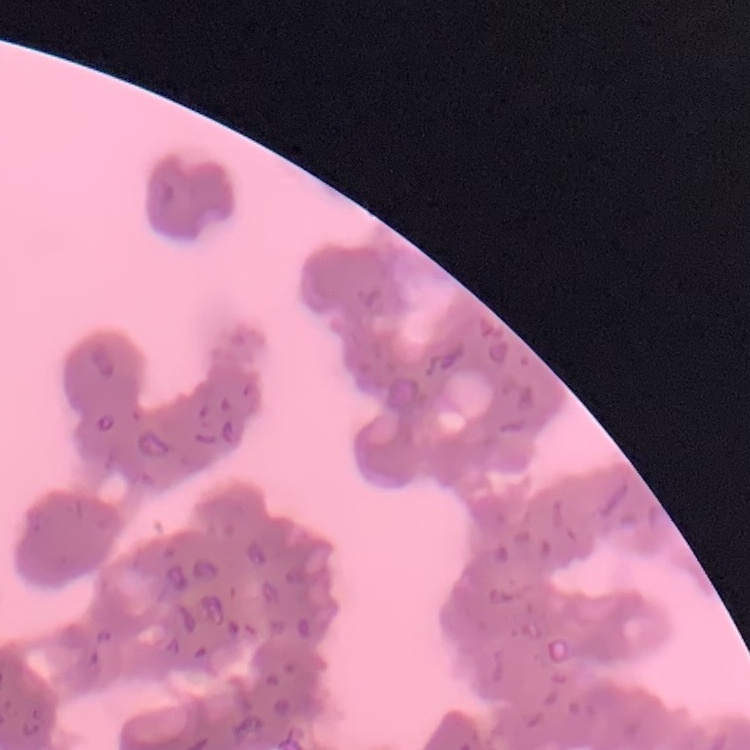

The erythrocytes show rouleaux formation. Field's or Giemsa stain. One tile cut from a larger photomicrograph. Thin blood film.